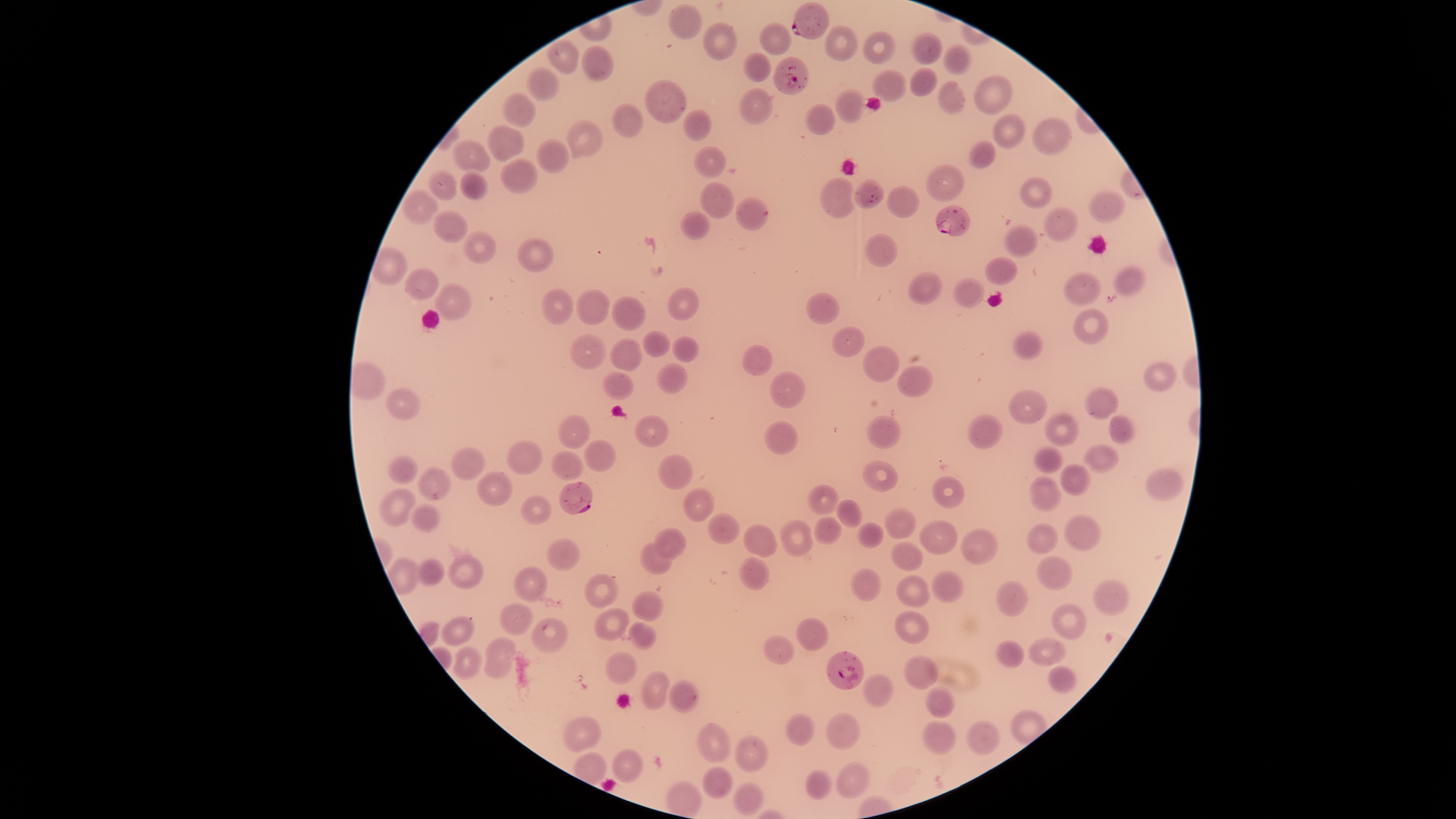

Approximate bounding boxes as (left, top, right, bottom) in pixels. Parasitized red blood cells: (793, 3, 830, 40), (774, 58, 810, 95), (936, 204, 970, 236), (560, 482, 593, 515), (827, 652, 864, 691). Uninfected red blood cells: (669, 5, 704, 40), (704, 22, 738, 61), (760, 23, 792, 55), (827, 25, 858, 61), (864, 32, 896, 64), (911, 33, 942, 65), (944, 44, 972, 75), (582, 46, 615, 83), (743, 53, 772, 82), (526, 68, 561, 101), (911, 68, 938, 96), (873, 70, 907, 102), (975, 75, 1012, 115), (646, 80, 686, 123), (939, 82, 966, 115), (740, 88, 774, 124), (835, 89, 865, 124), (501, 93, 537, 128), (613, 103, 644, 138), (804, 105, 837, 135), (684, 110, 711, 142), (993, 114, 1024, 150), (1034, 117, 1072, 157), (566, 120, 603, 159), (487, 124, 524, 164), (537, 139, 570, 174), (452, 140, 491, 176), (969, 140, 995, 170), (695, 147, 726, 178), (501, 157, 538, 194), (928, 163, 962, 202), (428, 171, 458, 200), (460, 171, 488, 201), (821, 177, 855, 219), (1021, 177, 1052, 209), (701, 183, 734, 220), (886, 186, 919, 217), (1090, 190, 1126, 224), (401, 191, 439, 224), (736, 198, 768, 232), (1044, 206, 1079, 243), (431, 211, 467, 243), (681, 212, 711, 240), (1004, 225, 1037, 258), (463, 232, 496, 264), (865, 234, 898, 267), (519, 238, 555, 273), (985, 257, 1018, 285), (1114, 266, 1145, 296), (405, 268, 439, 302), (908, 272, 941, 305), (1065, 273, 1100, 306), (954, 278, 984, 307), (434, 284, 472, 322), (543, 288, 573, 325), (667, 288, 699, 321), (577, 289, 610, 326), (805, 293, 840, 325), (613, 297, 646, 331), (1074, 310, 1108, 345), (832, 325, 865, 357), (643, 330, 670, 358), (1013, 331, 1043, 360), (570, 335, 608, 370), (673, 337, 698, 363), (610, 339, 642, 373), (743, 344, 773, 376), (863, 346, 900, 382), (1145, 362, 1176, 392), (657, 364, 688, 395), (898, 366, 932, 397), (770, 372, 806, 410), (602, 373, 634, 401), (1086, 387, 1118, 419), (385, 389, 420, 420), (1009, 390, 1048, 425), (1045, 413, 1079, 446), (967, 414, 1003, 451), (558, 415, 591, 450), (867, 415, 902, 449), (1109, 415, 1135, 445), (636, 416, 668, 447), (765, 421, 799, 455), (507, 440, 543, 476), (585, 440, 616, 473), (1084, 445, 1119, 473), (450, 448, 485, 481), (1033, 448, 1063, 473), (551, 450, 584, 482), (659, 453, 693, 490), (388, 455, 417, 485), (861, 461, 899, 491), (1060, 463, 1091, 496), (417, 468, 451, 502), (1145, 468, 1184, 502), (476, 472, 513, 506), (932, 477, 965, 508), (1029, 478, 1062, 511), (806, 485, 839, 515), (683, 488, 714, 522), (379, 489, 416, 527), (521, 495, 551, 526), (837, 500, 862, 528), (410, 504, 441, 532), (884, 509, 916, 540), (707, 513, 739, 545), (1064, 515, 1100, 550), (813, 518, 842, 544), (780, 521, 815, 556), (917, 521, 958, 555), (857, 523, 884, 549), (1027, 523, 1058, 555), (744, 524, 777, 558), (655, 528, 688, 560), (961, 528, 998, 564), (547, 538, 579, 571), (639, 542, 675, 576), (890, 542, 925, 572), (449, 555, 483, 588), (1037, 556, 1072, 591), (741, 557, 769, 592), (416, 558, 444, 586), (513, 567, 548, 602), (852, 568, 882, 602), (930, 571, 964, 603), (585, 573, 618, 607), (897, 576, 930, 607), (1095, 579, 1128, 616), (997, 581, 1029, 618), (633, 590, 664, 622), (499, 603, 533, 635), (1053, 603, 1086, 640), (595, 608, 630, 639), (895, 610, 929, 644), (440, 616, 476, 645), (533, 618, 569, 653), (795, 618, 828, 651), (629, 622, 657, 649), (762, 635, 795, 664), (483, 637, 513, 678), (1028, 637, 1066, 666), (996, 640, 1024, 669), (452, 647, 481, 679), (607, 651, 636, 683), (903, 655, 939, 689), (1049, 667, 1076, 693), (641, 670, 670, 710), (862, 674, 893, 708), (668, 680, 699, 713), (927, 687, 955, 718), (787, 713, 816, 746), (827, 713, 859, 749), (563, 716, 601, 751), (924, 721, 955, 755), (967, 721, 1000, 756), (697, 723, 732, 763), (736, 735, 769, 773), (612, 750, 644, 784), (836, 762, 869, 799), (702, 767, 734, 799), (806, 769, 831, 801), (734, 783, 764, 816). The visible region is circular. Giemsa-stained preparation. Species: Plasmodium falciparum. Image is 1456×819 pixels. Presence: malaria parasites identified. Single field of view. Photographed with a smartphone camera through the microscope eyepiece. Thin smear of blood.